Locate every blood parasite and identify its species.
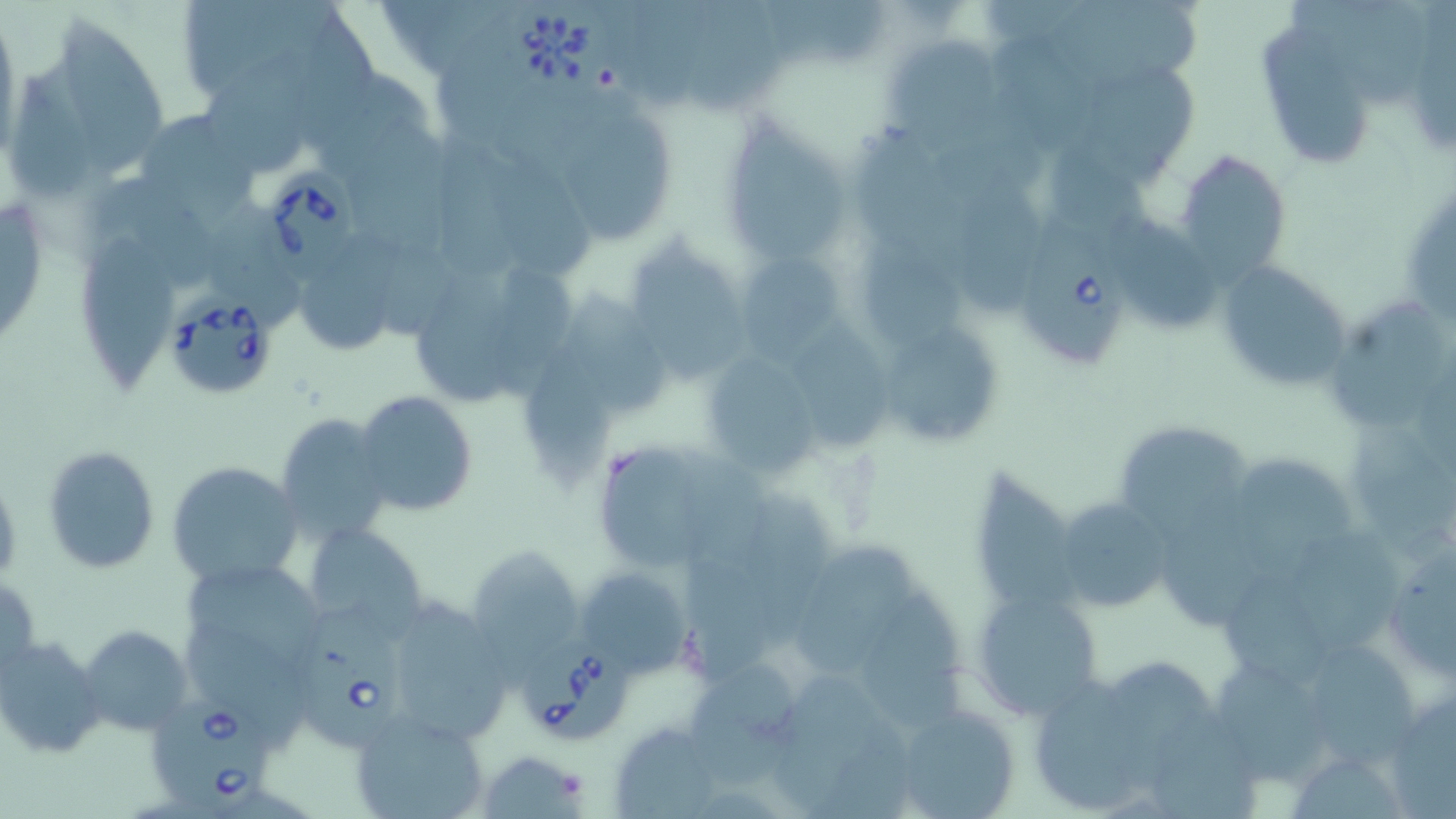

Approximate bounding boxes as (x1, y1, x2, y2) in pixels.
Babesia divergens-infected red blood cells: (507, 1, 612, 95), (259, 156, 354, 286), (1015, 215, 1130, 377), (163, 295, 279, 400), (298, 608, 403, 752), (520, 634, 631, 739), (147, 689, 268, 815).
No Plasmodium falciparum, Plasmodium ovale, Plasmodium malariae, Plasmodium vivax, or Trypanosoma brucei observed.

Summary:
  - Uninfected red blood cell locations: (176, 0, 352, 112), (629, 0, 728, 113), (696, 1, 788, 108), (768, 1, 888, 70), (1055, 1, 1209, 86), (1333, 1, 1433, 114), (0, 12, 21, 164), (64, 19, 164, 176), (1257, 26, 1371, 166), (995, 35, 1101, 159), (888, 36, 1004, 154), (207, 45, 318, 172), (1087, 65, 1200, 189), (13, 73, 97, 206), (500, 85, 604, 173), (138, 107, 256, 218), (567, 108, 677, 241), (730, 115, 848, 268), (356, 121, 452, 259), (436, 126, 524, 287), (865, 129, 977, 271), (487, 146, 598, 282), (1173, 149, 1290, 283), (960, 182, 1045, 317), (101, 183, 218, 286), (1110, 212, 1234, 333), (309, 231, 411, 353), (77, 234, 186, 388), (623, 241, 749, 381), (738, 246, 848, 363), (1215, 261, 1355, 389), (491, 263, 582, 407), (419, 264, 517, 405), (579, 291, 668, 418), (1327, 295, 1449, 429), (797, 311, 900, 456), (877, 320, 1001, 449), (522, 335, 617, 488), (714, 350, 819, 479), (354, 391, 480, 517), (276, 411, 393, 546), (1343, 416, 1456, 565), (1112, 421, 1256, 540), (587, 437, 745, 572), (41, 445, 160, 575), (1242, 453, 1361, 584), (167, 460, 302, 591), (977, 465, 1082, 617), (747, 494, 853, 656), (1053, 495, 1175, 615), (304, 523, 430, 637), (1167, 529, 1268, 627), (1296, 530, 1413, 653), (795, 531, 919, 674), (1382, 540, 1456, 681), (686, 545, 775, 684), (464, 546, 586, 666), (190, 564, 323, 670), (576, 564, 692, 673), (2, 574, 41, 681), (1230, 583, 1328, 693), (971, 587, 1104, 718), (857, 588, 967, 740), (378, 594, 515, 745), (189, 621, 319, 743), (77, 624, 193, 736), (0, 637, 106, 759), (1309, 642, 1424, 763), (1114, 659, 1233, 790), (691, 660, 801, 782), (1223, 660, 1329, 784), (779, 670, 879, 807), (1037, 670, 1141, 816), (1382, 683, 1455, 814), (1153, 700, 1256, 819), (892, 704, 1022, 819), (352, 711, 488, 819), (610, 722, 725, 818), (478, 750, 589, 817), (1295, 755, 1408, 819)
  - Slide-level diagnosis: Babesia divergens
  - Magnification: 1000x
  - Modality: light microscopy
  - Preparation: thin blood film
  - Field of view: single
  - Image size: 1456×819 pixels
  - Stain: May-Grünwald-Giemsa